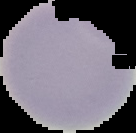

preparation = thin blood film
malaria status = uninfected
image size = 136×133 pixels
image type = segmented cell region with the area outside set to black